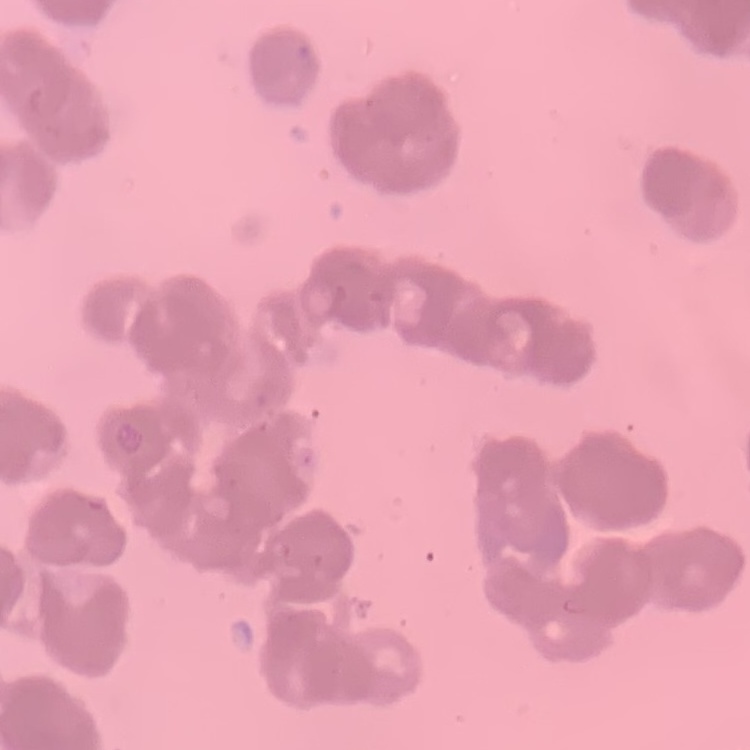
The red blood cells exhibit rouleaux formation. Thin peripheral smear. Stained with either Field's or Giemsa. Square crop of a larger photomicrograph.